Classify this cell by malaria status.
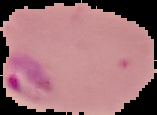
It is parasitized.

Summary:
  - Image type: segmented cell region on a black background
  - Preparation: thin blood smear
  - Image size: 157×115 pixels